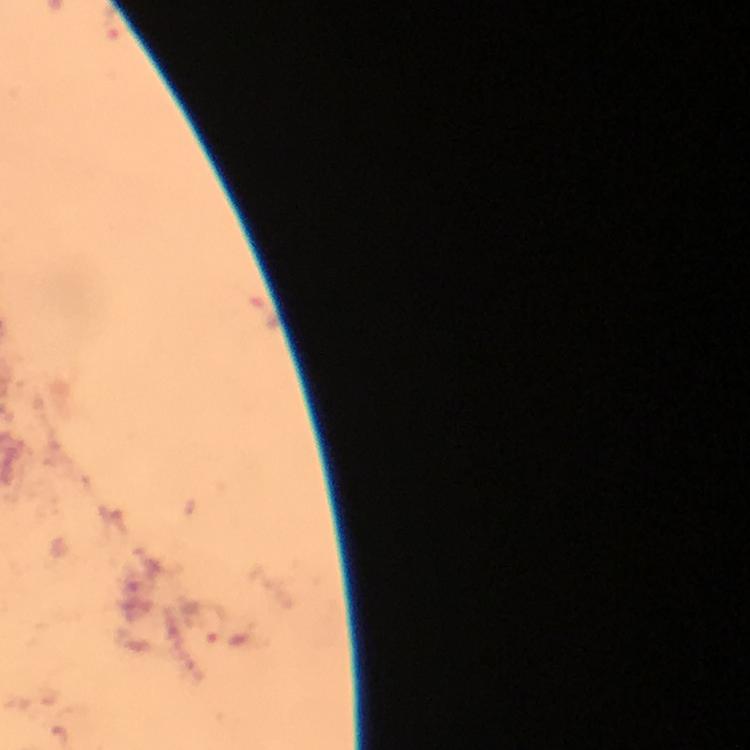
{
  "cropped_from": "a single field of view",
  "stain": "Giemsa",
  "magnification": "100x",
  "capture": "smartphone mounted on the microscope",
  "image_size": "750×750 pixels",
  "context": "from a diagnostic examination for malaria",
  "immersion_oil": "applied",
  "plasmodium_parasite_locations": "approximate object centers, in pixels from the top-left corner: (x=113, y=21)",
  "preparation": "thick blood smear"
}